Locate every Plasmodium parasite.
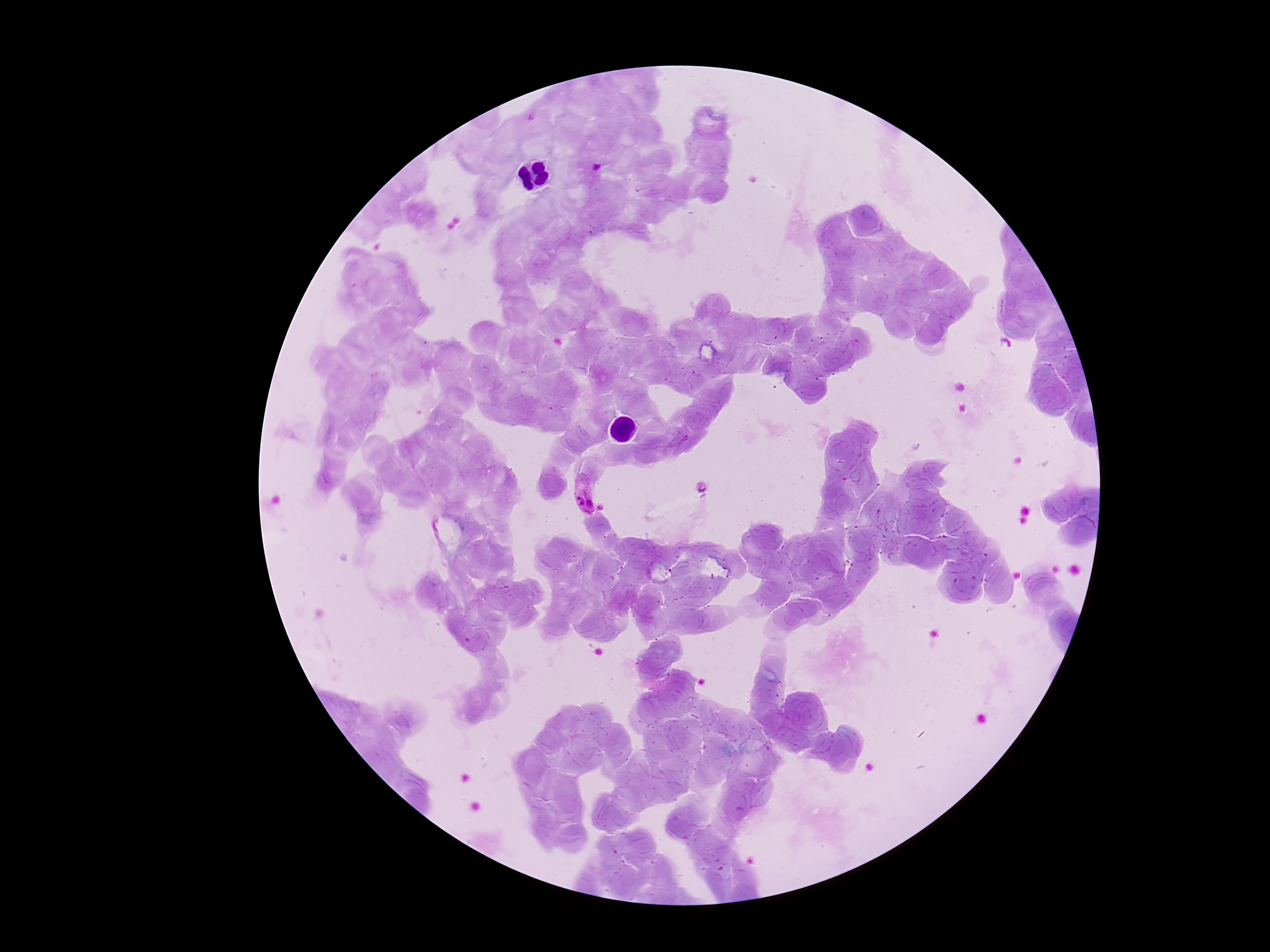
Approximate centers as {x, y} in pixels.
Plasmodium parasites: {596, 169}, {581, 493}.

Summary:
  - Field of view: single
  - Image size: 1270×952 pixels
  - Capture: smartphone camera through the microscope eyepiece
  - Preparation: thick peripheral-blood smear
  - Magnification: 100x
  - Stain: Giemsa
  - Patient malaria status: infected